Assess this cell for malaria.
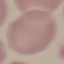
It is uninfected.

Thin blood smear. Giemsa-stained preparation. Photographed with a smartphone camera at the microscope eyepiece. Cell patch, automatically extracted from a larger field of view and resized to 64 × 64 pixels.